Give the position of every Plasmodium parasite visible.
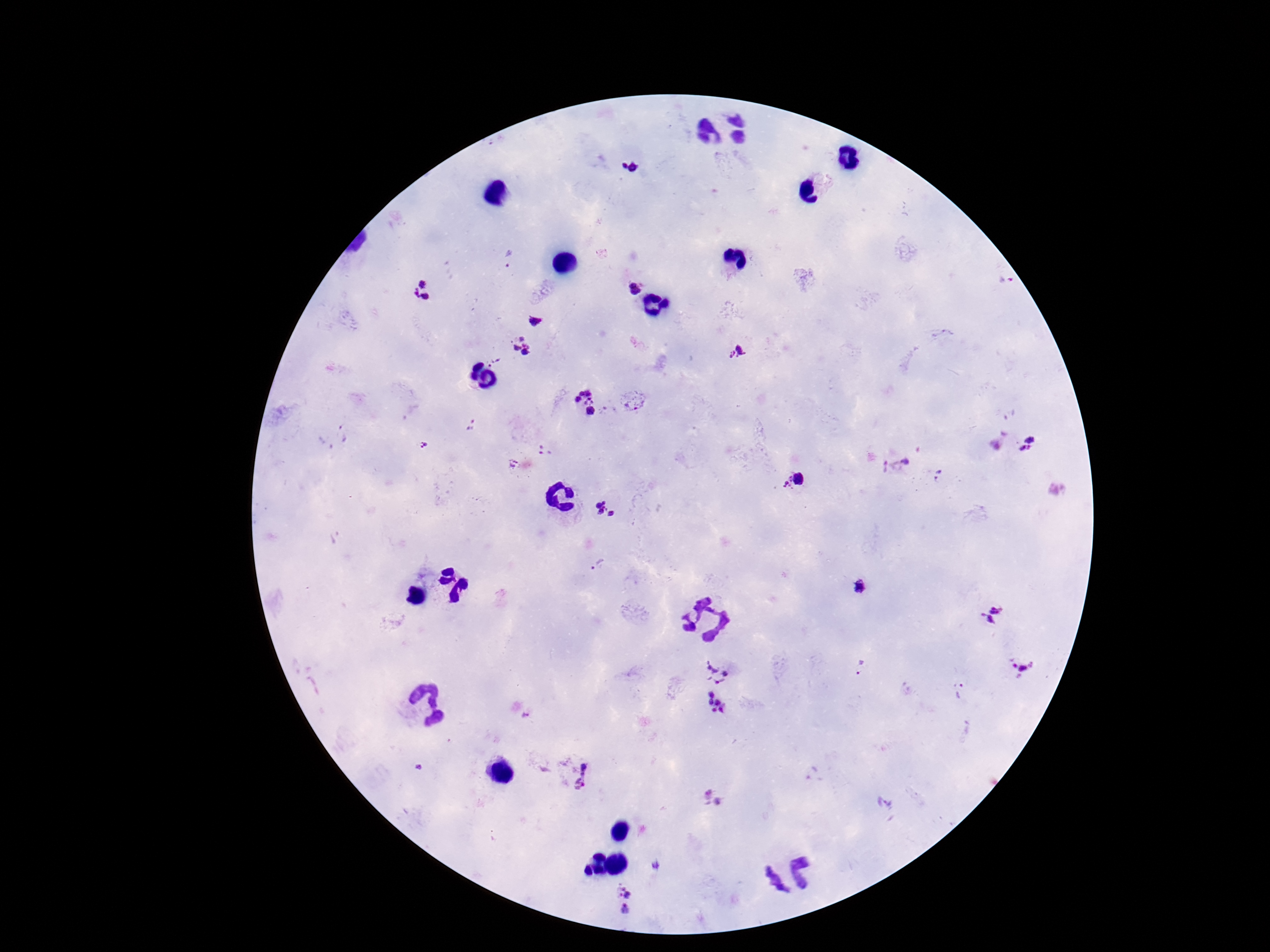
Approximate centers as (x, y) in pixels.
Plasmodium parasites: (628, 165), (509, 259), (633, 288), (422, 292), (537, 321), (523, 346), (736, 353), (495, 360), (634, 401), (584, 404), (472, 426), (340, 434), (424, 444), (1029, 446), (544, 450), (509, 464), (895, 467), (939, 476), (793, 479), (606, 508), (598, 566), (858, 588), (994, 615), (723, 666), (861, 667), (1020, 667), (960, 691), (716, 704), (526, 717), (584, 777), (712, 796), (657, 867), (624, 898).

Patient malaria status: infected. Giemsa-stained preparation. Photographed through the microscope eyepiece with a smartphone camera. Image is 1270×952 pixels. Thick blood film. One field from this slide. 100x magnification.